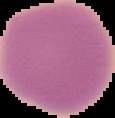 From a thin blood film. Result: no Plasmodium parasites detected. Cell region segmented out of the field of view; the surrounding area is masked to black. Image is 115×118 pixels.